Describe the morphology of the red blood cells.
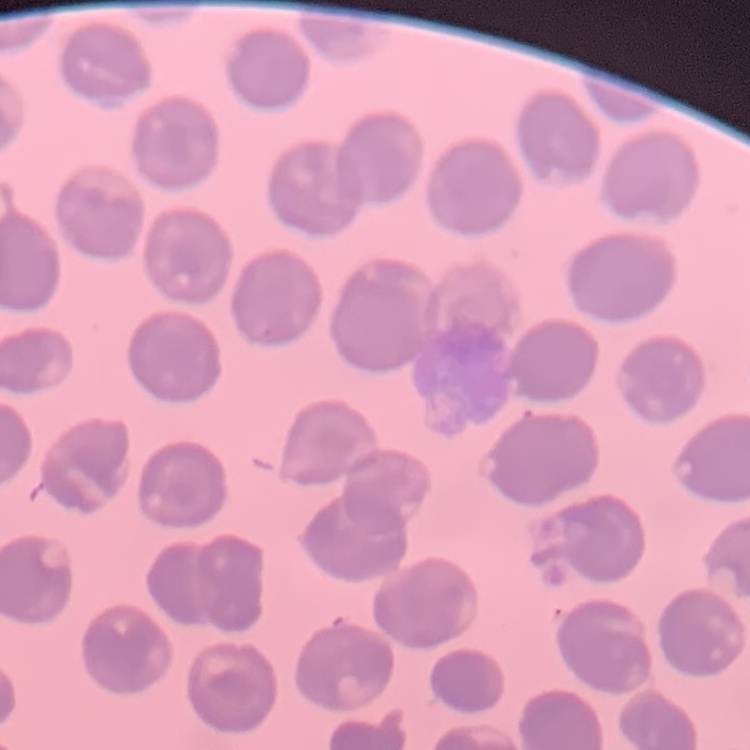
They show no rouleaux formation.

Summary:
  - Stain: Field's or Giemsa
  - Image type: one tile cut from a larger photomicrograph
  - Preparation: thin blood smear